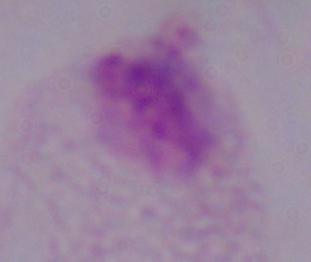

{
  "identification": "trichomonad",
  "magnification": "1000x",
  "modality": "photomicrograph"
}